Classify this cell by malaria status.
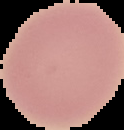

Uninfected.

Image is 124×130 pixels. From a thin blood smear. Cell region segmented out of the field of view; the surrounding area is masked to black.